Assess this cell for malaria.
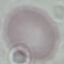
It is uninfected.

Summary:
  - Preparation: thin blood film
  - Stain: Giemsa
  - Capture: smartphone through the microscope eyepiece
  - Image type: automatically extracted cell patch, resized to 64 × 64 pixels